Classify this cell by malaria status.
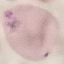

It is parasitized.

Automatically extracted cell patch, resized to 64 × 64 pixels. Giemsa-stained preparation. Thin smear of blood. Acquired by smartphone through the microscope eyepiece.